Give the extent of all uninfected red blood cells.
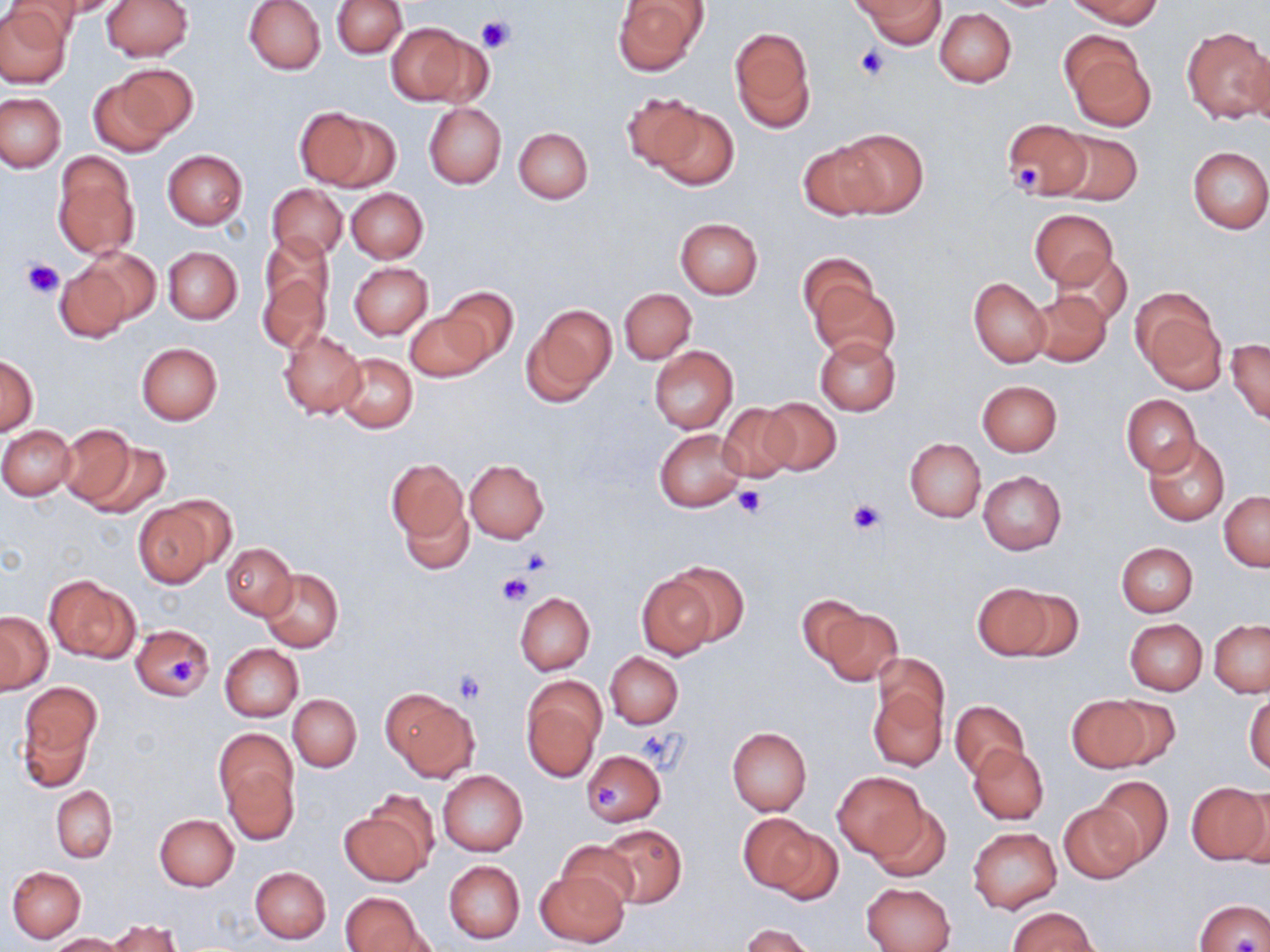
Approximate bounding boxes as (x1,y1)-(x2,y2) corner pairs in pixels.
Uninfected red blood cells: (46,0)-(127,18), (102,0)-(194,61), (244,0)-(326,75), (332,0)-(407,58), (613,0)-(709,76), (1068,0)-(1162,30), (855,1)-(943,49), (0,2)-(72,88), (933,7)-(1017,88), (387,24)-(472,104), (1183,27)-(1268,125), (729,28)-(817,134), (1059,28)-(1155,131), (1245,44)-(1270,136), (94,69)-(192,155), (621,91)-(710,172), (0,92)-(66,172), (423,103)-(506,189), (647,105)-(738,191), (294,106)-(392,190), (1000,119)-(1093,201), (513,126)-(593,203), (831,127)-(927,218), (1050,128)-(1143,206), (796,139)-(891,221), (1187,146)-(1270,234), (162,149)-(247,228), (52,152)-(139,260), (267,184)-(347,260), (346,188)-(428,264), (1029,209)-(1119,288), (675,218)-(763,298), (163,246)-(242,323), (78,247)-(160,329), (1052,250)-(1131,328), (799,252)-(876,331), (257,260)-(329,354), (349,262)-(433,339), (54,263)-(131,343), (807,275)-(899,363), (969,277)-(1051,368), (437,286)-(520,365), (619,287)-(696,364), (1029,289)-(1112,367), (1132,289)-(1226,394), (522,304)-(617,403), (406,308)-(492,382), (278,328)-(366,418), (815,336)-(901,417), (1226,338)-(1270,425), (136,343)-(223,424), (649,345)-(739,434), (335,353)-(417,433), (0,355)-(38,434), (976,379)-(1062,457), (1121,395)-(1202,475), (757,397)-(842,477), (717,403)-(799,484), (56,423)-(142,511), (1,427)-(75,500), (655,429)-(747,513), (1143,436)-(1230,525), (80,437)-(172,519), (905,439)-(986,521), (386,457)-(468,554), (464,460)-(548,543), (978,471)-(1066,554), (1219,493)-(1269,571), (400,497)-(474,576), (132,498)-(221,587), (1115,541)-(1198,616), (222,543)-(295,618), (658,560)-(749,649), (261,568)-(343,652), (637,573)-(720,660), (44,575)-(140,664), (973,583)-(1061,660), (515,592)-(595,675), (796,594)-(873,669), (813,605)-(903,687), (0,612)-(52,693), (1124,618)-(1207,695), (1209,620)-(1270,697), (132,624)-(214,702), (219,644)-(303,722), (605,652)-(683,728), (872,652)-(950,738), (520,678)-(605,779), (18,682)-(101,776), (869,682)-(946,772), (381,689)-(479,781), (1245,692)-(1269,775), (288,694)-(361,771), (1067,694)-(1159,772), (950,700)-(1027,781), (726,726)-(812,816), (216,734)-(298,838), (968,744)-(1049,825), (582,750)-(666,826), (438,770)-(528,856), (832,771)-(929,861), (1090,776)-(1172,866), (1186,781)-(1270,864), (52,787)-(117,862), (868,802)-(950,882), (1059,803)-(1146,883), (341,805)-(433,886), (738,813)-(825,898), (155,814)-(238,891), (598,824)-(687,908), (969,828)-(1061,913), (556,842)-(639,913), (444,860)-(525,943), (7,866)-(86,943), (251,866)-(330,944), (534,867)-(630,948), (862,882)-(955,952), (341,892)-(427,952), (1194,899)-(1269,951), (1008,907)-(1097,952), (109,920)-(180,952), (741,923)-(817,952), (50,933)-(130,951).

{
  "slide_level_diagnosis": "no evidence of blood parasites",
  "modality": "optical microscopy",
  "magnification": "1000x",
  "field_of_view": "single",
  "stain": "May-Grünwald-Giemsa",
  "preparation": "thin blood smear",
  "platelet_locations": "approximate bounding boxes as (x1,y1)-(x2,y2) corner pairs in pixels: (477,14)-(516,54), (852,42)-(893,82), (1015,160)-(1040,188), (21,259)-(64,298), (733,487)-(765,518), (846,498)-(887,535), (521,546)-(555,575), (497,572)-(530,606), (166,657)-(198,685), (457,668)-(488,703), (636,730)-(680,769), (592,781)-(622,809)",
  "image_size": "1270×952 pixels"
}